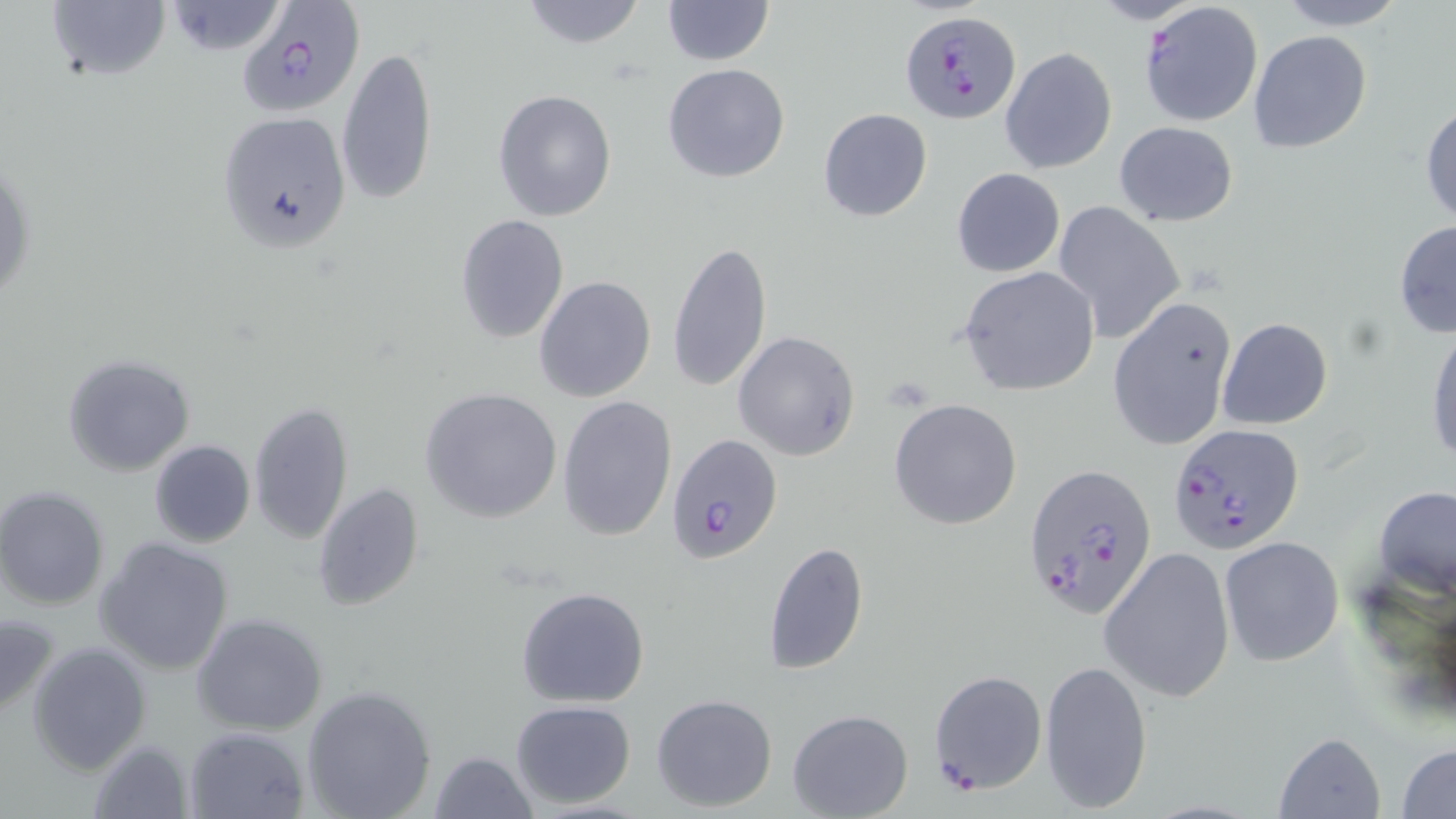
Summary:
  - Coordinate format: approximate bounding boxes as (x1, y1, x2, y2) in pixels
  - Plasmodium falciparum-infected red blood cell locations: (235, 2, 364, 117), (1138, 2, 1264, 128), (901, 12, 1019, 123), (1169, 423, 1303, 554), (666, 434, 782, 564), (1021, 463, 1158, 622)
  - Uninfected red blood cell locations: (42, 0, 172, 85), (517, 0, 649, 49), (661, 0, 775, 66), (1273, 0, 1409, 30), (161, 2, 290, 55), (1248, 30, 1372, 154), (337, 46, 437, 208), (1000, 47, 1117, 174), (663, 63, 791, 183), (493, 90, 617, 222), (1421, 99, 1456, 227), (818, 108, 931, 222), (216, 111, 351, 252), (1112, 122, 1239, 226), (1, 144, 36, 315), (951, 168, 1065, 278), (1052, 203, 1186, 344), (456, 214, 569, 342), (1393, 218, 1455, 339), (666, 239, 771, 393), (958, 266, 1100, 396), (533, 275, 656, 403), (1105, 297, 1236, 450), (1216, 317, 1333, 429), (1426, 318, 1456, 469), (733, 330, 860, 461), (62, 352, 195, 476), (421, 386, 563, 523), (556, 394, 679, 543), (888, 397, 1022, 529), (250, 400, 353, 544), (149, 440, 256, 549), (313, 483, 425, 610), (1373, 484, 1455, 594), (1, 487, 113, 610), (1218, 535, 1345, 667), (94, 536, 234, 676), (763, 542, 870, 677), (1099, 545, 1236, 704), (515, 587, 650, 708), (0, 612, 59, 720), (191, 613, 330, 735), (27, 641, 152, 775), (1039, 658, 1152, 813), (929, 670, 1046, 793), (301, 684, 438, 819), (650, 693, 778, 812), (510, 699, 636, 807), (789, 709, 912, 819), (184, 726, 310, 818), (1273, 731, 1385, 817), (85, 737, 194, 818), (1396, 742, 1456, 818), (429, 750, 539, 819)
  - Slide-level diagnosis: Plasmodium falciparum
  - Modality: light microscopy
  - Stain: May-Grünwald-Giemsa
  - Magnification: 1000x
  - Image size: 1456×819 pixels
  - Field of view: single
  - Preparation: thin blood smear